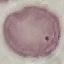

Malaria status: uninfected. Thin blood smear. Cell patch, automatically extracted from a larger field of view and resized to 64 × 64 pixels. Photographed with a smartphone camera at the microscope eyepiece. Giemsa stain.